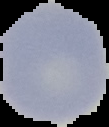

Summary:
  - Malaria status: uninfected
  - Image size: 109×127 pixels
  - Preparation: thin blood smear
  - Image type: segmented cell region on a black background